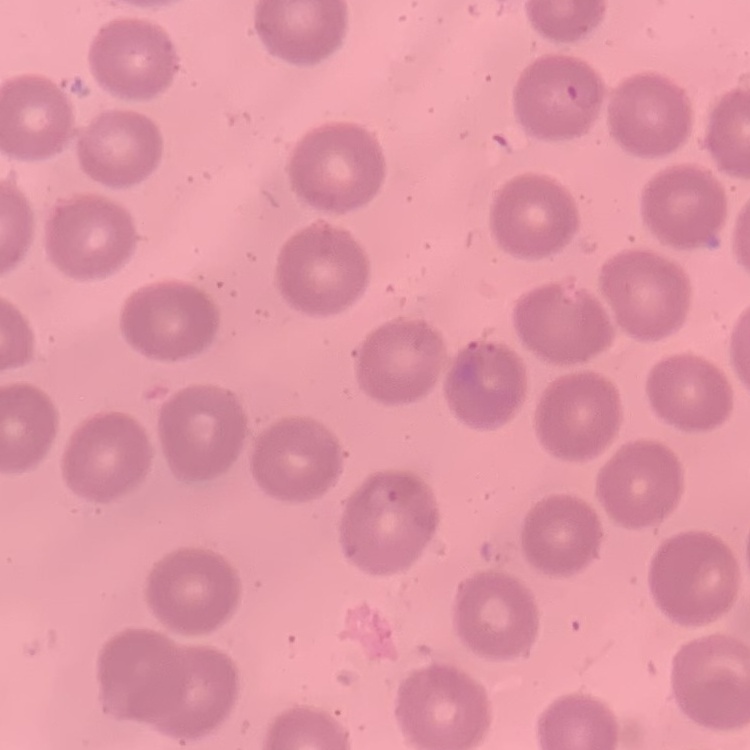
The erythrocytes exhibit no rouleaux formation. One tile cut from a larger photomicrograph. Thin blood smear. Stained with either Field's or Giemsa.